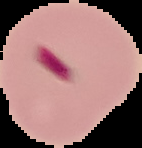

Malaria status: parasitized. Image is 142×148 pixels. From a thin blood film. The area outside the segmented cell region is set to black.